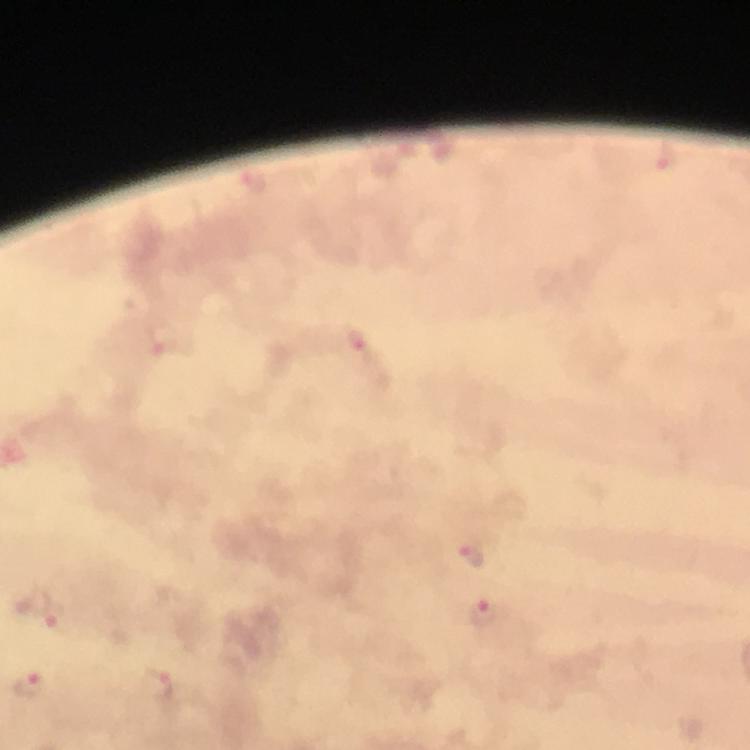
capture = smartphone camera through the microscope
magnification = 100x
context = from a diagnostic examination for malaria
immersion oil = applied
cropped from = one field of view
stain = Giemsa
image size = 750×750 pixels
Plasmodium parasite locations = approximate object centers, in pixels from the top-left corner: (x=667, y=159), (x=163, y=337), (x=355, y=342), (x=473, y=555), (x=484, y=612), (x=53, y=616)
preparation = thick blood smear